Identify the blood parasite species.
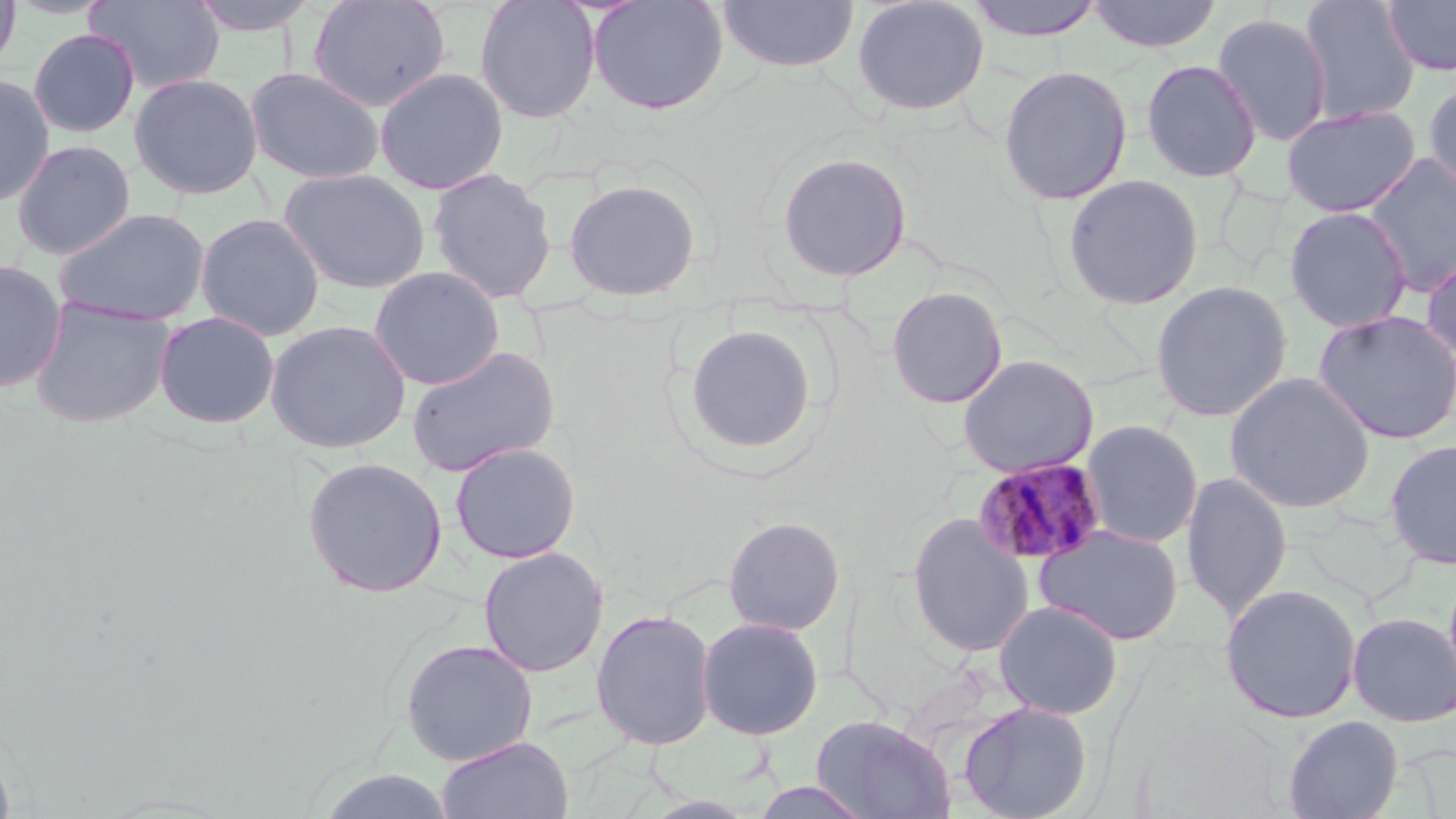

Plasmodium malariae.

stain: May-Grünwald-Giemsa
preparation: thin blood smear
image_size: 1456×819 pixels
magnification: 1000x
modality: light microscopy
field_of_view: single
uninfected_red_blood_cell_locations: 'approximate bounding boxes as (x1,y1)-(x2,y2) corner pairs in pixels: (0,0)-(21,77), (85,0)-(225,94), (185,0)-(323,38), (307,0)-(451,112), (474,0)-(602,124), (587,0)-(730,115), (715,0)-(861,74), (852,0)-(990,117), (967,0)-(1105,42), (1087,0)-(1222,53), (1381,0)-(1456,77), (1298,1)-(1420,124), (1211,12)-(1333,147), (28,28)-(141,138), (1140,59)-(1262,182), (997,64)-(1133,206), (244,66)-(386,185), (374,67)-(509,194), (128,71)-(264,199), (0,72)-(56,207), (1423,78)-(1456,198), (1281,105)-(1421,217), (11,139)-(136,260), (775,151)-(913,282), (1362,153)-(1456,297), (278,167)-(431,294), (426,168)-(558,305), (1062,173)-(1204,311), (562,178)-(701,301), (1283,205)-(1413,333), (51,207)-(211,327), (194,212)-(326,342), (1420,248)-(1456,369), (0,258)-(68,393), (368,265)-(505,391), (1149,280)-(1293,423), (885,285)-(1008,409), (29,297)-(176,428), (1311,309)-(1456,445), (153,310)-(280,430), (264,320)-(412,455), (684,324)-(817,456), (405,344)-(561,477), (956,353)-(1099,479), (1223,371)-(1376,513), (1079,419)-(1204,549), (1384,438)-(1456,570), (449,441)-(581,564), (301,456)-(448,598), (1181,471)-(1292,622), (905,512)-(1035,658), (722,515)-(846,636), (1033,525)-(1185,645), (477,546)-(609,677), (1442,562)-(1456,703), (1219,583)-(1363,724), (993,600)-(1124,720), (590,608)-(717,750), (1346,612)-(1456,726), (696,616)-(824,741), (399,638)-(538,766), (958,700)-(1093,819), (811,714)-(957,819), (1283,714)-(1404,819), (436,736)-(575,819), (0,738)-(16,819), (317,768)-(457,819), (747,780)-(877,818)'
plasmodium_malariae_infected_red_blood_cell_locations: 'approximate bounding boxes as (x1,y1)-(x2,y2) corner pairs in pixels: (972,457)-(1108,567)'